Name the parasite shown.
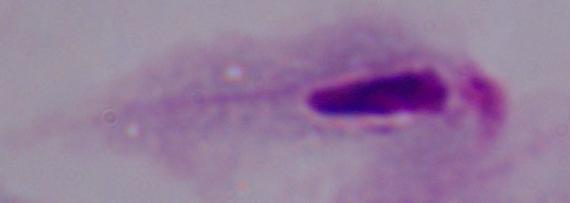

This is a trichomonad.

{
  "magnification": "1000x",
  "modality": "micrograph"
}